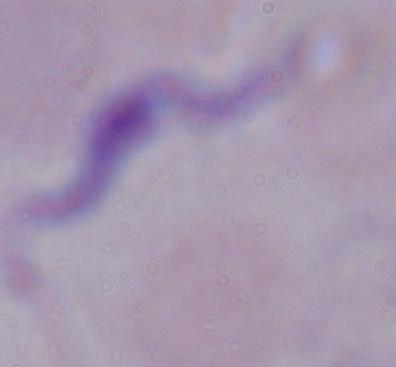 A trypanosome is shown. 1000x magnification. Photomicrograph.